Outline each blood parasite and name the species.
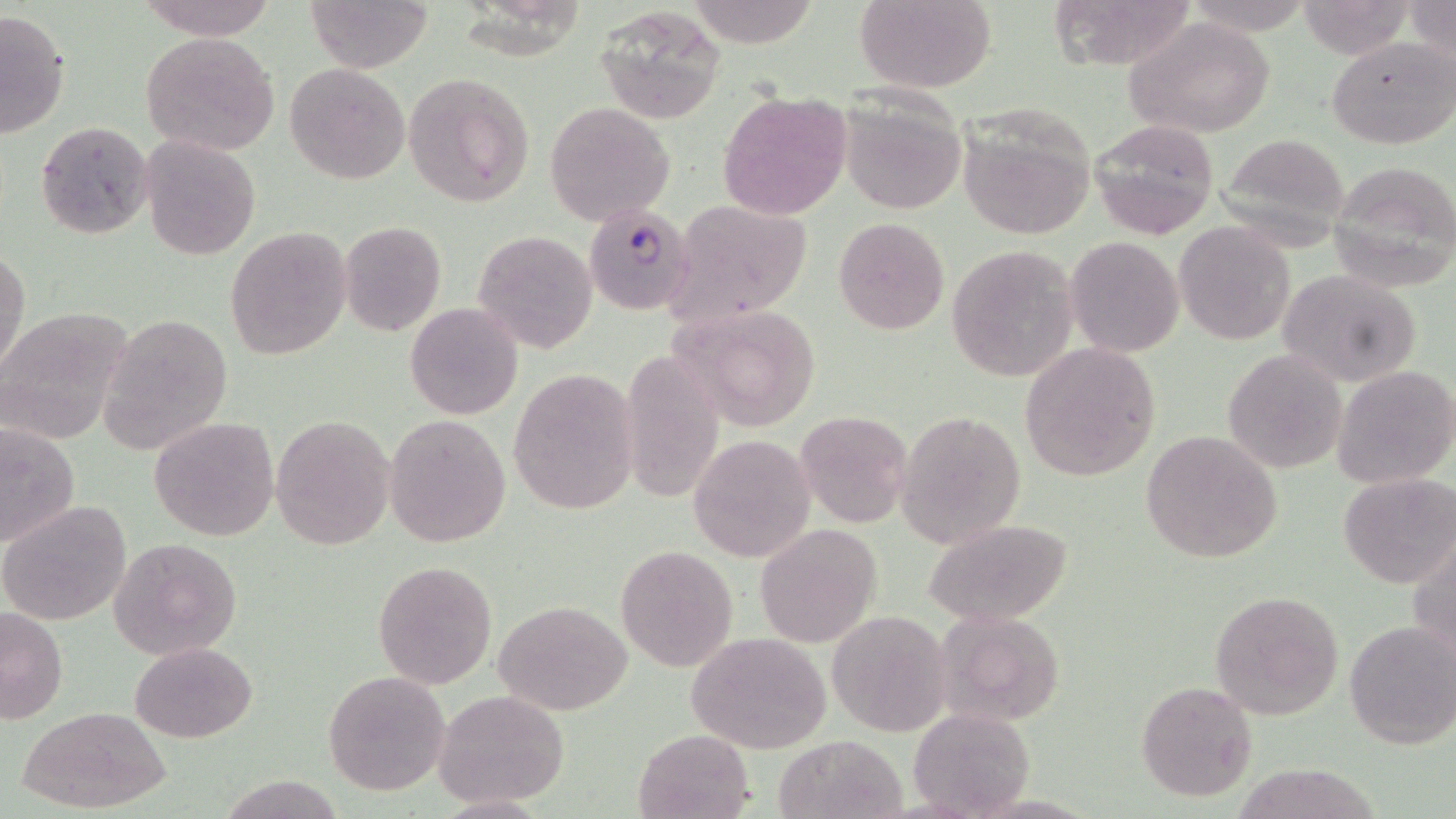

Approximate bounding boxes as [x1, y1, x2, y2] in pixels.
Plasmodium falciparum-infected red blood cells: [585, 205, 696, 313].
No Plasmodium ovale, Plasmodium malariae, Plasmodium vivax, Babesia divergens, or Trypanosoma brucei observed.

Uninfected red blood cell locations: [138, 0, 276, 39], [307, 0, 433, 71], [686, 0, 823, 48], [853, 0, 997, 91], [1047, 0, 1200, 70], [1294, 1, 1418, 60], [1407, 1, 1455, 71], [593, 6, 725, 122], [1, 10, 71, 136], [1123, 16, 1277, 137], [139, 32, 280, 156], [1326, 36, 1455, 149], [285, 62, 410, 185], [401, 72, 536, 209], [837, 87, 969, 216], [718, 92, 851, 219], [543, 102, 675, 225], [957, 107, 1098, 240], [36, 120, 154, 240], [1089, 120, 1219, 239], [1214, 133, 1354, 249], [140, 134, 262, 261], [1327, 161, 1456, 292], [661, 199, 817, 327], [833, 217, 950, 335], [340, 221, 447, 335], [1174, 223, 1295, 345], [224, 226, 352, 361], [472, 230, 598, 353], [1064, 236, 1184, 357], [945, 246, 1078, 382], [1, 248, 29, 378], [1280, 269, 1423, 387], [670, 301, 821, 431], [404, 302, 522, 419], [0, 309, 131, 443], [99, 313, 234, 455], [1018, 344, 1161, 481], [619, 348, 727, 504], [1221, 348, 1349, 476], [1333, 364, 1456, 489], [508, 368, 641, 516], [795, 410, 914, 529], [895, 410, 1026, 547], [271, 413, 396, 551], [384, 413, 512, 548], [149, 417, 279, 541], [0, 422, 80, 549], [1140, 430, 1282, 563], [688, 435, 814, 561], [1337, 472, 1455, 591], [0, 501, 131, 625], [923, 519, 1074, 626], [756, 522, 882, 647], [1410, 533, 1456, 668], [108, 538, 242, 659], [614, 543, 739, 673], [371, 559, 497, 689], [1211, 588, 1344, 720], [495, 601, 631, 715], [0, 607, 68, 724], [936, 609, 1065, 728], [827, 612, 950, 735], [1343, 620, 1455, 750], [686, 632, 833, 753], [130, 642, 257, 742], [321, 670, 451, 796], [1136, 678, 1259, 803], [433, 690, 569, 807], [19, 706, 174, 813], [908, 706, 1033, 816], [634, 728, 754, 819], [773, 733, 908, 819], [223, 775, 344, 818], [432, 795, 551, 818]. Slide-level diagnosis: Plasmodium falciparum. Image is 1456×819 pixels. Thin blood film. Captured at 1000x magnification. Optical microscopy. May-Grünwald-Giemsa stain. Single field of view.